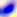
Summary:
  - Magnification: 400x
  - Identification: Toxoplasma gondii
  - Modality: micrograph